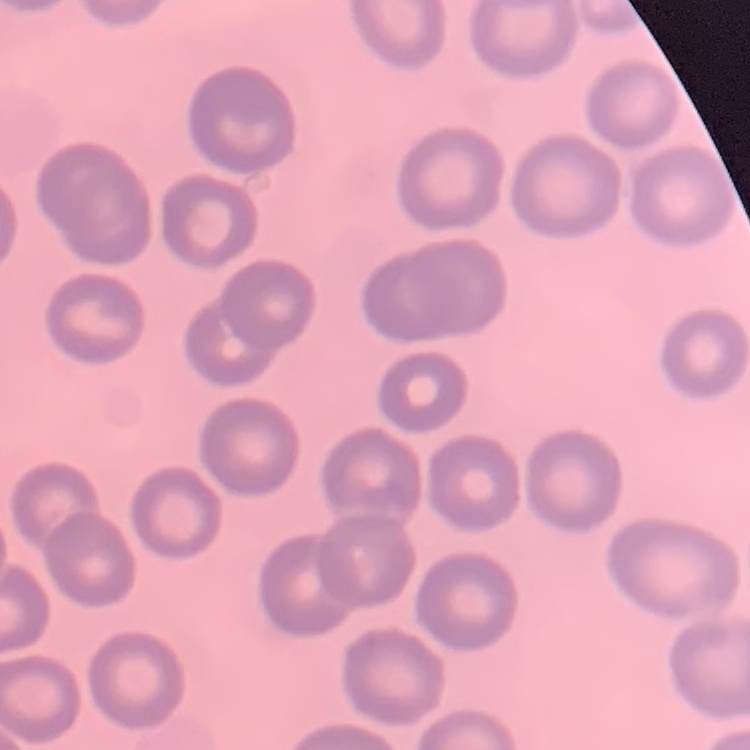

The erythrocytes show no rouleaux formation. Field's or Giemsa stain. Thin blood film. Square crop of a larger photomicrograph.